Outline each Plasmodium vivax-infected red blood cell.
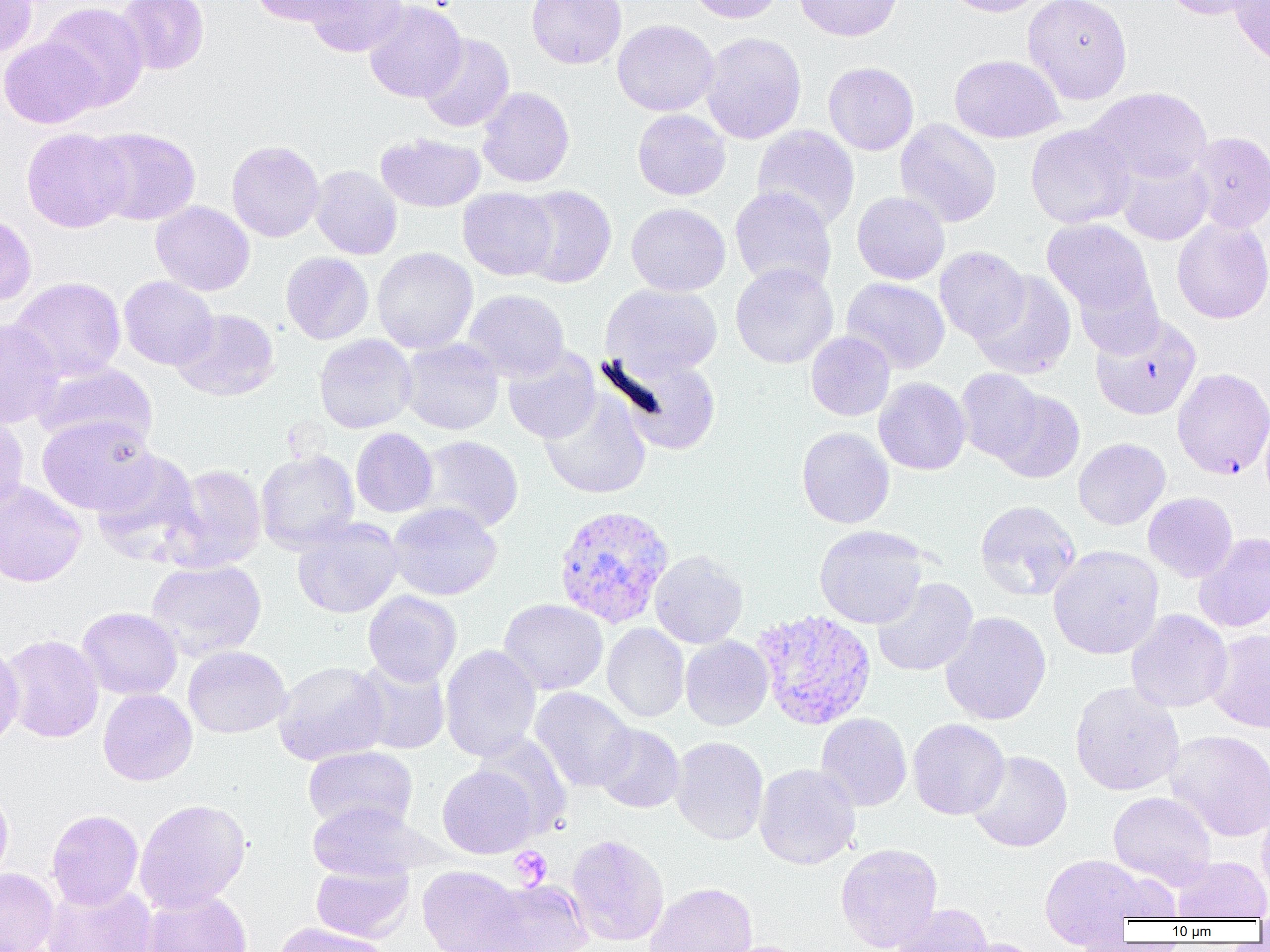

Approximate bounding boxes as (x1, y1, x2, y2) in pixels.
Plasmodium vivax-infected red blood cells: (553, 505, 674, 629), (752, 609, 877, 730).

Uninfected red blood cell locations: (116, 0, 209, 75), (250, 0, 356, 26), (304, 0, 408, 57), (527, 0, 626, 69), (686, 0, 784, 24), (794, 0, 903, 41), (941, 0, 1048, 17), (1022, 0, 1133, 104), (1160, 0, 1261, 20), (0, 1, 38, 58), (363, 1, 466, 103), (1229, 1, 1270, 68), (41, 2, 148, 111), (612, 19, 719, 116), (701, 32, 806, 144), (418, 33, 515, 133), (0, 37, 101, 129), (949, 54, 1065, 143), (823, 62, 919, 155), (477, 86, 575, 188), (1086, 87, 1213, 186), (632, 109, 731, 200), (895, 118, 1002, 227), (1025, 123, 1138, 229), (751, 125, 860, 231), (86, 127, 201, 226), (21, 128, 132, 233), (1187, 131, 1270, 233), (376, 133, 485, 212), (226, 140, 325, 242), (1115, 155, 1213, 245), (309, 165, 402, 260), (514, 185, 617, 288), (730, 186, 837, 293), (458, 188, 558, 280), (852, 192, 950, 284), (151, 202, 255, 296), (626, 203, 731, 296), (0, 210, 36, 307), (1171, 217, 1270, 324), (1041, 218, 1156, 320), (934, 246, 1030, 342), (372, 247, 478, 353), (280, 252, 374, 344), (730, 262, 839, 369), (970, 270, 1077, 379), (1074, 273, 1164, 359), (119, 276, 218, 370), (10, 277, 126, 382), (841, 277, 950, 374), (602, 283, 723, 378), (463, 289, 569, 382), (172, 308, 280, 401), (1090, 315, 1202, 420), (0, 318, 64, 429), (806, 331, 895, 421), (314, 334, 417, 433), (399, 338, 504, 435), (503, 348, 600, 444), (609, 352, 723, 455), (35, 360, 157, 450), (955, 368, 1045, 462), (1172, 368, 1270, 480), (873, 377, 970, 475), (539, 389, 651, 498), (990, 390, 1085, 484), (1259, 402, 1270, 507), (0, 411, 29, 515), (36, 414, 158, 515), (796, 426, 894, 529), (351, 428, 438, 517), (414, 435, 524, 533), (1073, 438, 1170, 530), (256, 449, 360, 553), (91, 450, 205, 564), (167, 464, 267, 571), (0, 480, 87, 588), (1143, 492, 1237, 582), (974, 500, 1081, 601), (387, 502, 503, 601), (292, 518, 404, 618), (814, 525, 929, 629), (1194, 533, 1270, 633), (1048, 545, 1164, 659), (649, 550, 748, 649), (146, 559, 267, 660), (871, 577, 978, 677), (363, 590, 462, 686), (498, 598, 608, 695), (76, 607, 182, 700), (1126, 609, 1233, 713), (940, 611, 1052, 725), (602, 623, 689, 722), (1207, 629, 1270, 733), (2, 634, 104, 743), (680, 636, 773, 730), (0, 640, 24, 750), (183, 645, 291, 738), (440, 645, 542, 761), (351, 657, 451, 755), (273, 660, 390, 765), (1069, 682, 1185, 796), (530, 687, 637, 791), (98, 689, 197, 786), (815, 713, 912, 811), (908, 718, 1010, 820), (593, 723, 685, 813), (1165, 729, 1270, 841), (472, 734, 573, 838), (670, 736, 769, 845), (303, 746, 418, 833), (967, 750, 1072, 853), (754, 763, 860, 870), (437, 764, 539, 858), (0, 784, 13, 886), (1108, 790, 1216, 889), (134, 798, 251, 912), (307, 800, 430, 882), (1256, 802, 1270, 902), (46, 809, 144, 909), (565, 833, 670, 947), (22, 835, 103, 933), (835, 842, 943, 952), (1038, 853, 1150, 947), (1172, 856, 1270, 921), (311, 861, 414, 942), (417, 865, 525, 952), (0, 868, 59, 952), (1098, 870, 1182, 923), (477, 878, 593, 952), (42, 880, 158, 952), (645, 882, 757, 952), (140, 889, 252, 952), (891, 903, 994, 952), (276, 922, 390, 952), (959, 938, 1045, 952), (707, 940, 812, 952). Platelet locations: (510, 846, 552, 889). Slide-level diagnosis: Plasmodium vivax. Light microscopy. 1000x magnification. Single field of view. Image is 1270×952 pixels. Thin blood smear.